State the blood parasite species.
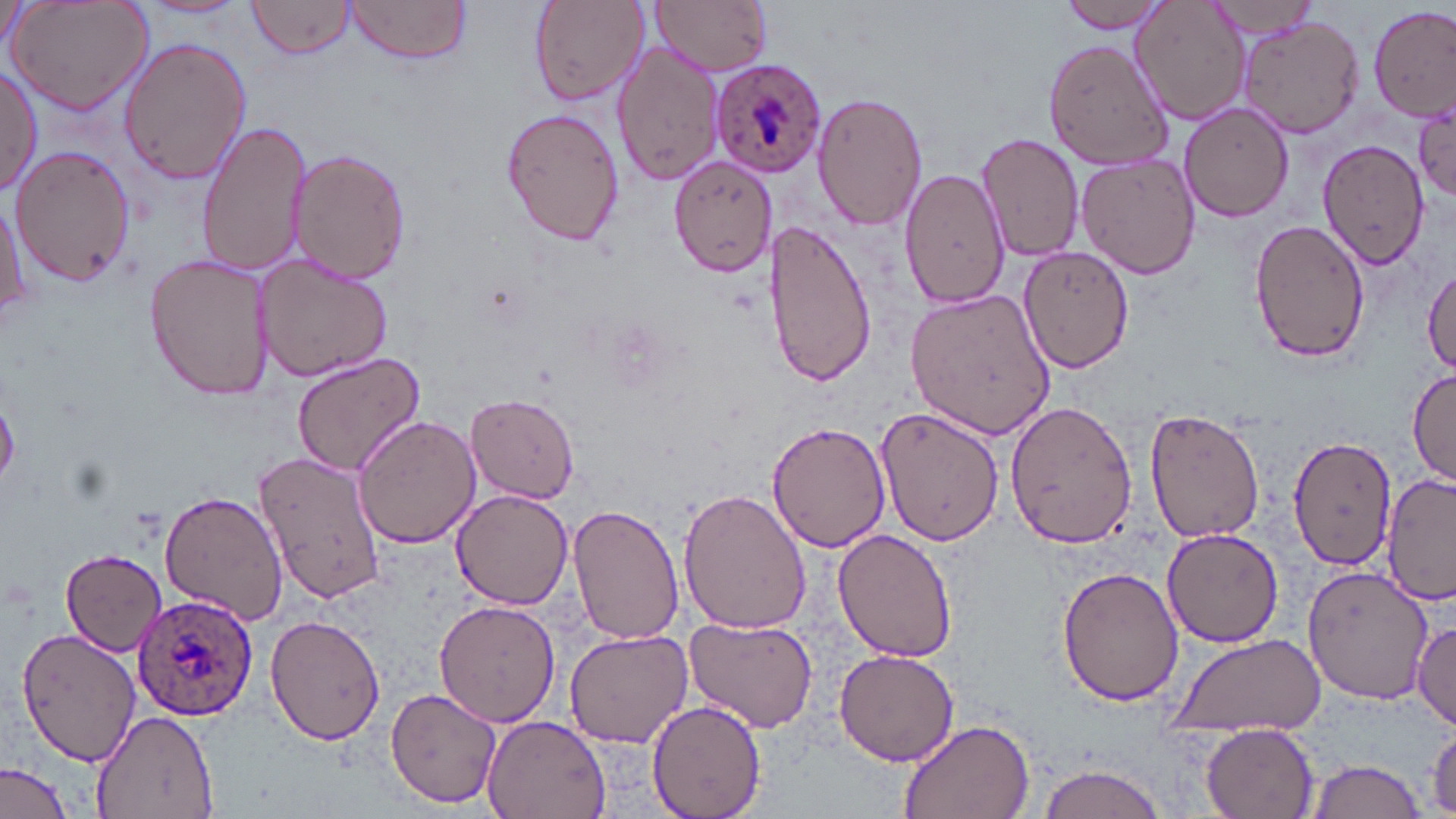

Plasmodium ovale.

uninfected_red_blood_cell_locations: 'approximate bounding boxes as named x1/y1/x2/y2 corners in pixels: (x1=6, y1=0, x2=154, y2=116), (x1=140, y1=0, x2=246, y2=18), (x1=247, y1=0, x2=358, y2=61), (x1=344, y1=0, x2=473, y2=68), (x1=650, y1=0, x2=772, y2=76), (x1=1056, y1=0, x2=1173, y2=33), (x1=1130, y1=1, x2=1248, y2=126), (x1=1202, y1=1, x2=1328, y2=41), (x1=527, y1=2, x2=647, y2=107), (x1=1369, y1=6, x2=1455, y2=122), (x1=1236, y1=14, x2=1363, y2=139), (x1=118, y1=36, x2=252, y2=184), (x1=1044, y1=38, x2=1175, y2=169), (x1=611, y1=39, x2=728, y2=188), (x1=0, y1=64, x2=42, y2=198), (x1=812, y1=90, x2=926, y2=230), (x1=1178, y1=102, x2=1294, y2=222), (x1=500, y1=105, x2=625, y2=248), (x1=1413, y1=105, x2=1456, y2=201), (x1=195, y1=119, x2=306, y2=278), (x1=976, y1=133, x2=1085, y2=261), (x1=1317, y1=139, x2=1429, y2=269), (x1=10, y1=144, x2=137, y2=286), (x1=290, y1=146, x2=410, y2=286), (x1=668, y1=154, x2=778, y2=278), (x1=1076, y1=154, x2=1202, y2=280), (x1=900, y1=168, x2=1009, y2=309), (x1=0, y1=195, x2=29, y2=322), (x1=1248, y1=217, x2=1373, y2=362), (x1=763, y1=218, x2=879, y2=390), (x1=1020, y1=245, x2=1135, y2=372), (x1=253, y1=252, x2=393, y2=383), (x1=146, y1=253, x2=273, y2=402), (x1=1421, y1=264, x2=1456, y2=375), (x1=907, y1=287, x2=1057, y2=441), (x1=290, y1=353, x2=425, y2=477), (x1=1408, y1=368, x2=1456, y2=482), (x1=466, y1=394, x2=581, y2=503), (x1=1004, y1=399, x2=1139, y2=550), (x1=1143, y1=405, x2=1270, y2=544), (x1=877, y1=406, x2=1003, y2=547), (x1=353, y1=415, x2=480, y2=548), (x1=767, y1=420, x2=890, y2=553), (x1=1288, y1=435, x2=1397, y2=571), (x1=255, y1=450, x2=387, y2=606), (x1=1384, y1=472, x2=1456, y2=608), (x1=157, y1=488, x2=289, y2=628), (x1=678, y1=488, x2=813, y2=636), (x1=450, y1=490, x2=575, y2=609), (x1=568, y1=505, x2=686, y2=647), (x1=1163, y1=528, x2=1286, y2=647), (x1=832, y1=529, x2=959, y2=663), (x1=58, y1=548, x2=168, y2=657), (x1=1304, y1=564, x2=1433, y2=705), (x1=1057, y1=566, x2=1183, y2=707), (x1=432, y1=600, x2=561, y2=727), (x1=266, y1=613, x2=386, y2=746), (x1=682, y1=616, x2=820, y2=733), (x1=1413, y1=619, x2=1455, y2=728), (x1=17, y1=627, x2=143, y2=765), (x1=563, y1=628, x2=695, y2=750), (x1=1167, y1=633, x2=1328, y2=738), (x1=834, y1=648, x2=961, y2=766), (x1=384, y1=688, x2=501, y2=809), (x1=646, y1=699, x2=767, y2=819), (x1=90, y1=709, x2=221, y2=818), (x1=480, y1=715, x2=610, y2=819), (x1=897, y1=716, x2=1036, y2=819), (x1=1200, y1=721, x2=1320, y2=819), (x1=1427, y1=722, x2=1456, y2=815), (x1=1307, y1=759, x2=1429, y2=818), (x1=0, y1=761, x2=74, y2=819), (x1=1034, y1=761, x2=1174, y2=819)'
plasmodium_ovale_infected_red_blood_cell_locations: 'approximate bounding boxes as named x1/y1/x2/y2 corners in pixels: (x1=710, y1=57, x2=829, y2=176), (x1=135, y1=592, x2=260, y2=720)'
field_of_view: one of a larger specimen
image_size: 1456×819 pixels
stain: May-Grünwald-Giemsa
magnification: 1000x
modality: optical microscopy
preparation: thin blood film